Locate every malaria parasite.
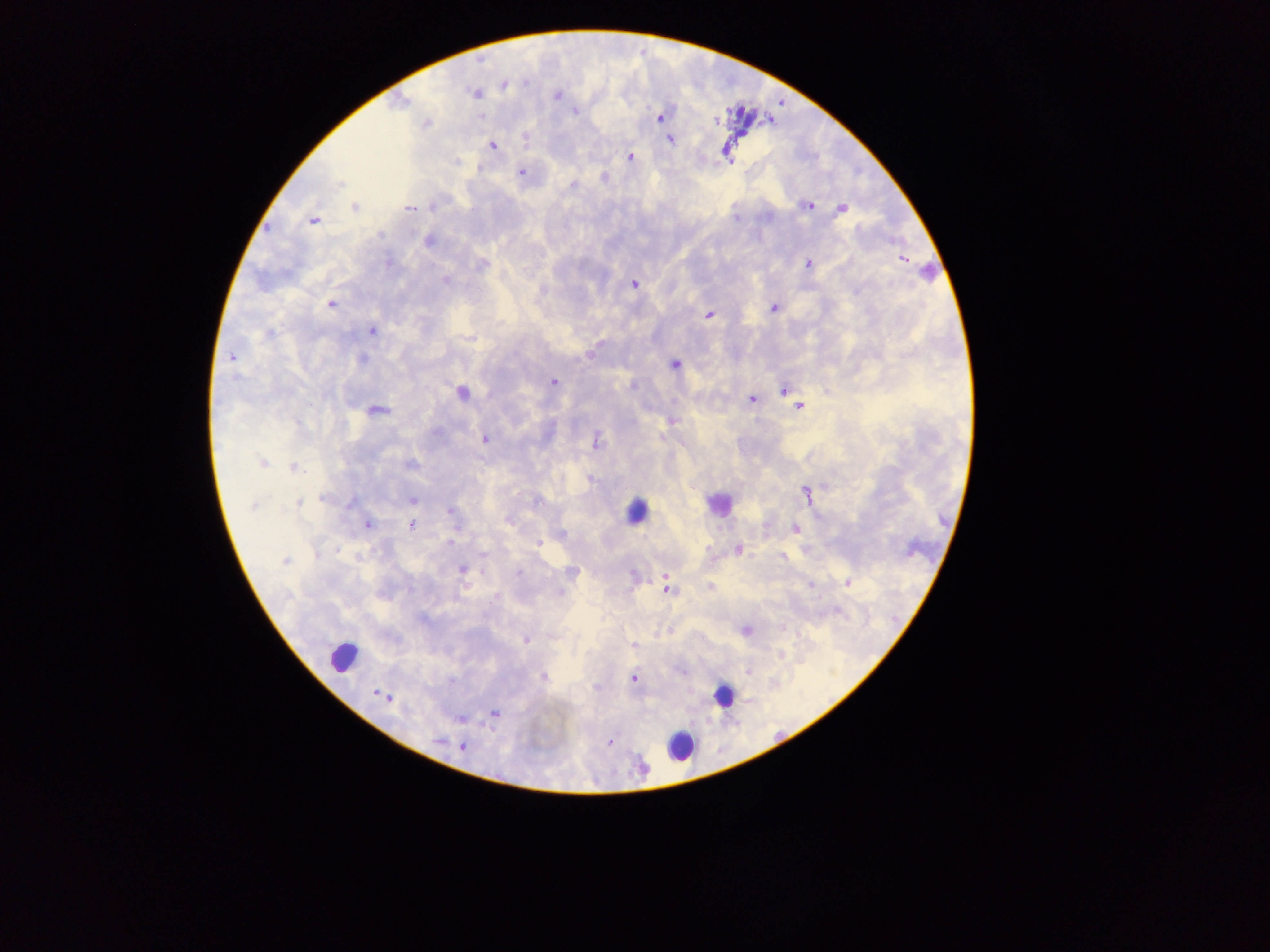
Approximate centers as [x, y] in pixels.
Malaria parasites: [528, 84], [504, 87], [474, 95], [555, 97], [575, 113], [661, 117], [427, 124], [528, 139], [671, 140], [494, 146], [630, 156], [456, 161], [522, 169], [574, 184], [812, 205], [843, 209], [410, 210], [313, 221], [428, 240], [902, 258], [807, 263], [447, 281], [634, 283], [331, 305], [773, 308], [708, 313], [370, 330], [271, 333], [469, 337], [589, 353], [231, 357], [362, 359], [675, 364], [553, 383], [632, 385], [782, 389], [462, 393], [752, 399], [799, 406], [377, 410], [671, 423], [484, 439], [598, 441], [263, 463], [411, 464], [292, 466], [806, 492], [323, 499], [412, 501], [350, 503], [298, 504], [254, 505], [449, 511], [368, 525], [411, 525], [796, 528], [452, 542], [539, 543], [364, 548], [738, 549], [340, 551], [360, 554], [316, 555], [783, 558], [285, 560], [462, 569], [520, 573], [574, 574], [665, 580], [846, 583], [814, 586], [709, 587], [560, 591], [494, 596], [782, 628], [747, 629], [527, 640], [632, 645], [782, 655], [748, 672], [543, 678], [633, 678], [495, 713], [460, 719], [608, 741], [463, 748].

Leukocyte locations: [636, 503], [717, 506], [345, 652], [722, 702], [678, 753]. Thick blood film. Image is 1270×952 pixels. One field of view. Sample from Ghana. Mobile-phone photograph taken through the microscope.